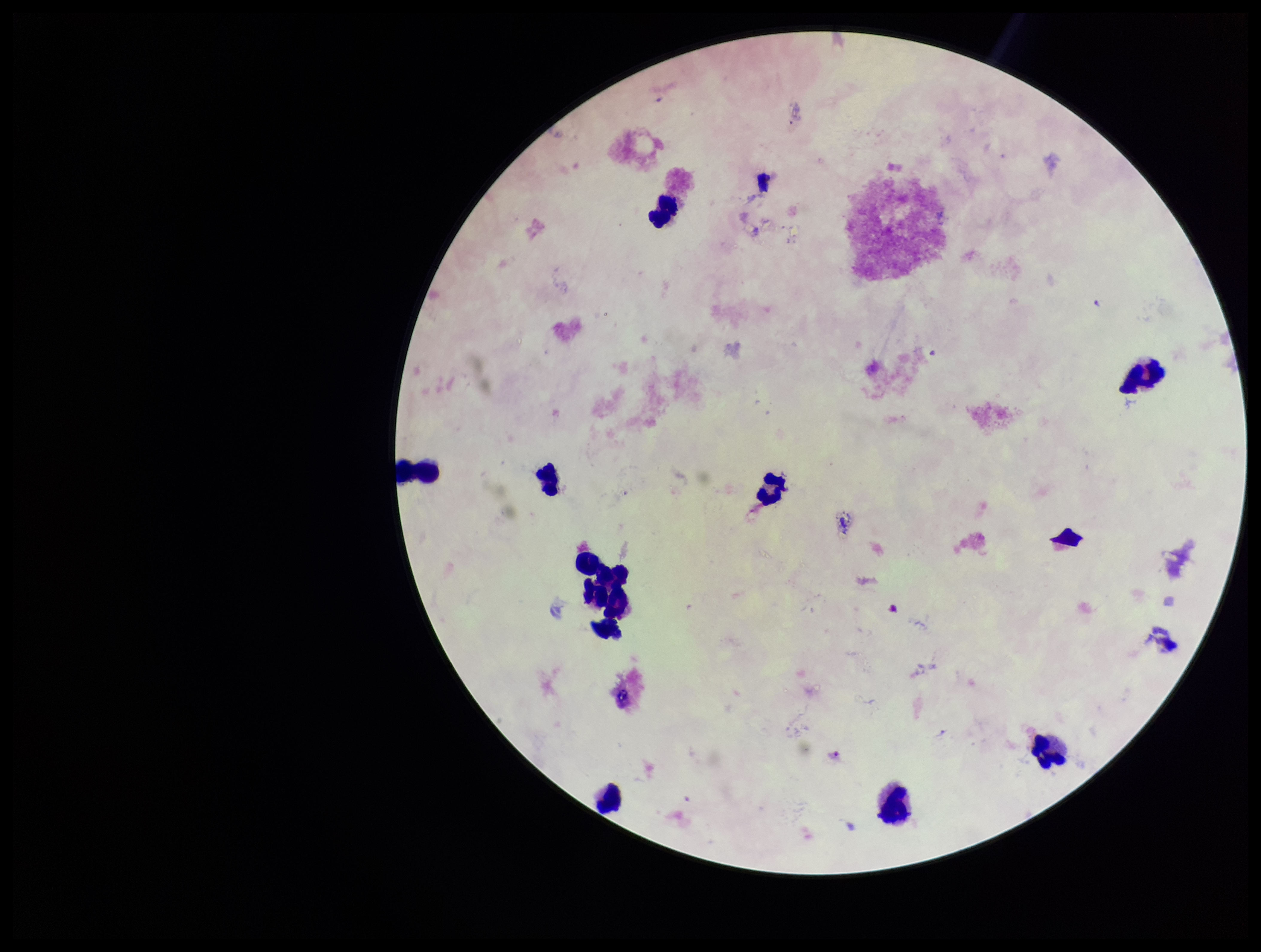
Summary:
  - Preparation: thick smear
  - Parasite count: 1
  - Image size: 1261×952 pixels
  - Capture: smartphone photograph through the microscope eyepiece
  - Stain: Giemsa
  - Leukocyte count: 12
  - Patient malaria status: infected
  - Species reported for this patient: Plasmodium falciparum
  - Plasmodium parasites: seen
  - Field of view: one from this slide